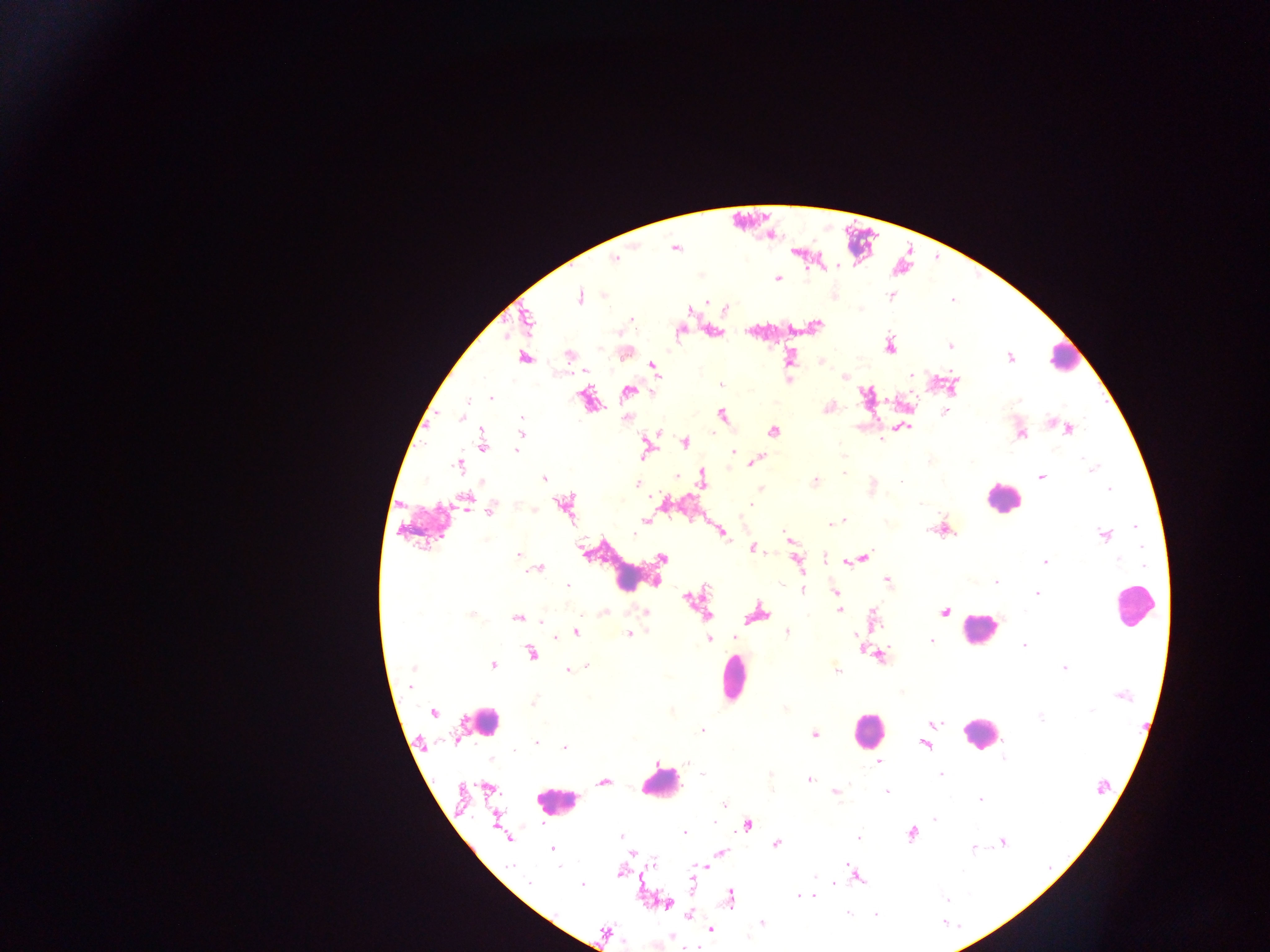
Approximate centers as {x, y} in pixels. Leukocyte locations: {1057, 365}, {1008, 503}, {1138, 605}, {980, 642}, {735, 680}, {476, 725}, {863, 732}, {987, 736}, {557, 802}. Malaria parasite locations: {834, 269}, {777, 279}, {578, 297}, {888, 297}, {948, 345}, {569, 356}, {790, 356}, {526, 358}, {1010, 358}, {822, 363}, {652, 365}, {843, 376}, {719, 385}, {954, 389}, {626, 392}, {864, 396}, {490, 398}, {828, 407}, {721, 415}, {908, 426}, {1069, 429}, {773, 432}, {520, 434}, {482, 435}, {881, 441}, {646, 442}, {685, 442}, {483, 443}, {735, 451}, {841, 454}, {761, 456}, {1086, 458}, {753, 462}, {460, 464}, {1094, 468}, {847, 472}, {701, 474}, {1042, 476}, {543, 478}, {815, 480}, {638, 484}, {759, 487}, {1107, 488}, {464, 500}, {748, 505}, {567, 508}, {489, 513}, {645, 519}, {843, 520}, {829, 524}, {944, 526}, {1135, 527}, {782, 532}, {721, 534}, {1104, 535}, {786, 537}, {752, 549}, {519, 554}, {865, 557}, {662, 558}, {1044, 561}, {797, 562}, {843, 562}, {539, 568}, {886, 581}, {654, 583}, {567, 584}, {803, 589}, {834, 591}, {1036, 594}, {684, 597}, {837, 611}, {645, 612}, {944, 612}, {761, 613}, {710, 614}, {872, 616}, {517, 617}, {788, 630}, {576, 631}, {629, 632}, {556, 636}, {855, 636}, {733, 637}, {709, 639}, {858, 639}, {930, 640}, {529, 652}, {877, 656}, {494, 665}, {568, 668}, {836, 669}, {1065, 670}, {434, 712}, {934, 725}, {701, 730}, {816, 735}, {536, 741}, {926, 743}, {564, 749}, {879, 762}, {941, 773}, {810, 779}, {603, 781}, {488, 786}, {886, 791}, {836, 792}, {979, 801}, {496, 816}, {935, 819}, {748, 825}, {685, 833}, {912, 834}, {621, 837}, {858, 837}, {1002, 841}, {775, 844}, {551, 848}, {972, 849}, {721, 852}, {632, 853}, {848, 862}, {706, 867}, {851, 868}, {618, 875}, {858, 877}, {835, 885}, {797, 895}, {813, 895}, {731, 897}, {947, 900}, {667, 903}, {846, 913}, {761, 921}, {709, 928}. Mobile-phone photograph taken through the microscope. Thick blood film. Sample from Ghana. Single field of view. Image is 1270×952 pixels.